Assess this cell for malaria.
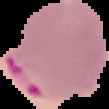

It is parasitized.

Summary:
  - Image type: cell region segmented out of the field of view; surrounding area masked to black
  - Preparation: thin blood film
  - Image size: 109×109 pixels